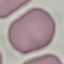
Malaria status: uninfected. Photographed with a smartphone camera at the microscope eyepiece. Thin blood film. Giemsa-stained preparation. Cell patch, automatically extracted from a larger field of view and resized to 64 × 64 pixels.